Describe the morphology of the red blood cells.
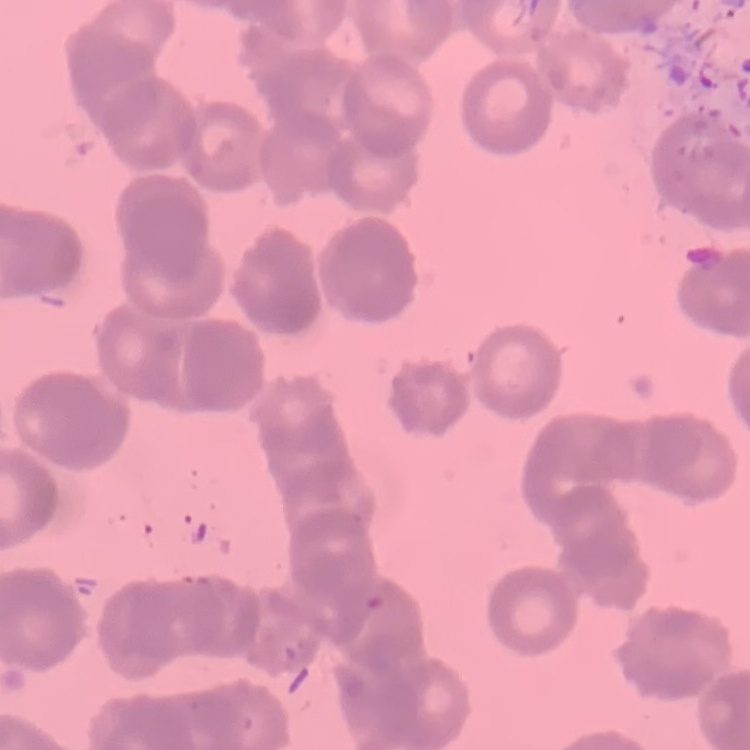

Rouleaux formation.

{
  "image_type": "square crop of a larger photomicrograph",
  "preparation": "thin peripheral smear",
  "stain": "Field's or Giemsa"
}